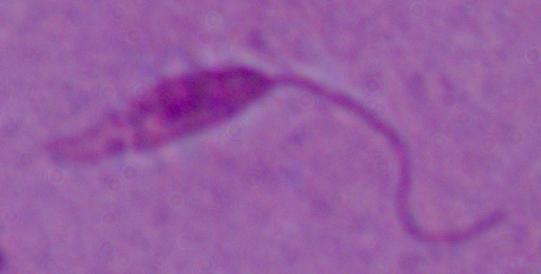

Summary:
  - Magnification: 1000x
  - Modality: photomicrograph
  - Identification: Leishmania